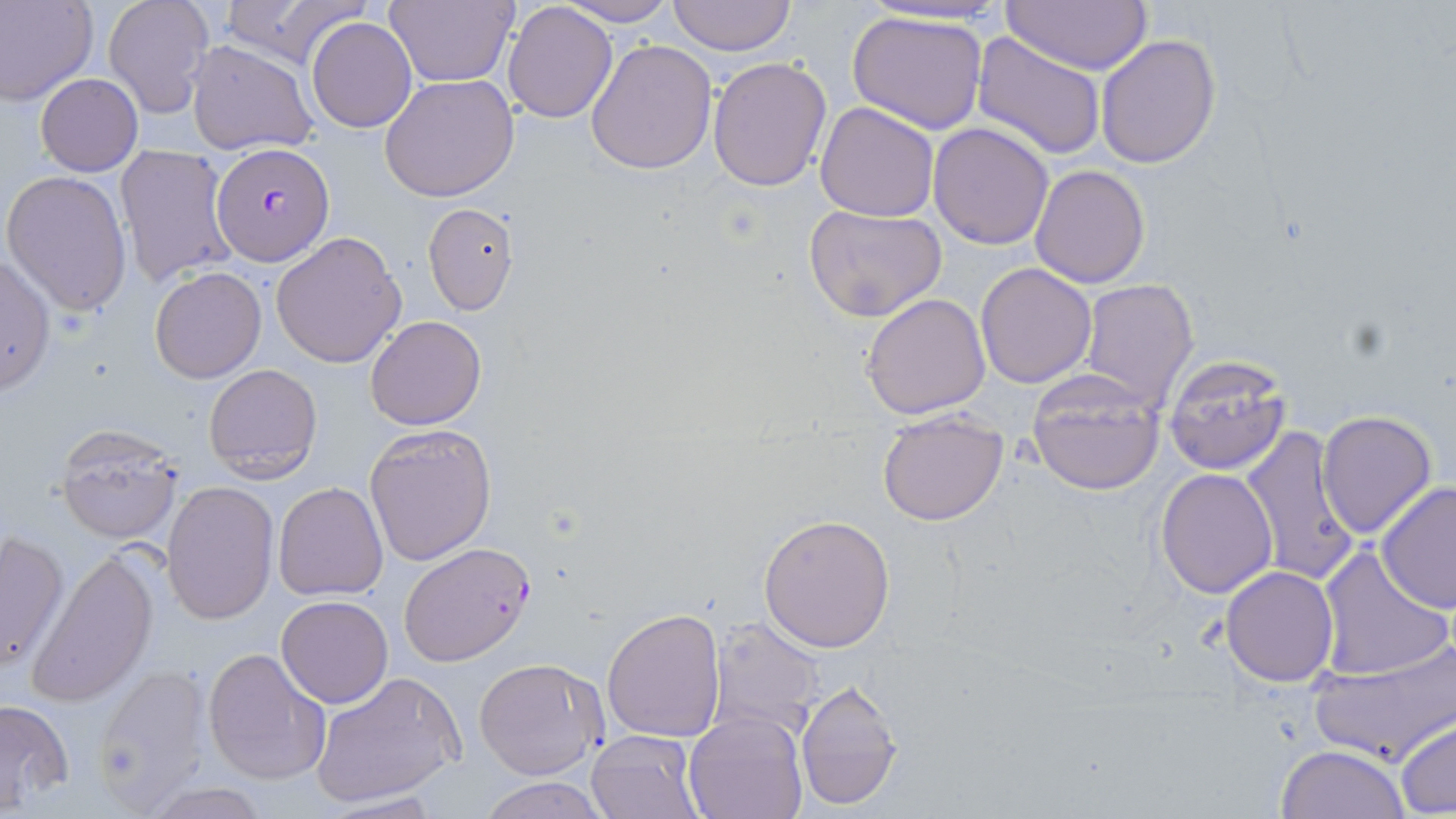
slide-level diagnosis = Plasmodium falciparum
stain = May-Grünwald-Giemsa
uninfected red blood cell locations = approximate bounding boxes as (x1, y1, x2, y2) in pixels: (0, 0, 97, 105), (217, 0, 371, 71), (385, 0, 514, 88), (666, 0, 797, 55), (101, 1, 214, 117), (558, 1, 677, 26), (999, 1, 1152, 73), (501, 3, 617, 122), (845, 9, 989, 134), (305, 18, 417, 133), (973, 33, 1107, 161), (1095, 35, 1221, 170), (585, 38, 717, 176), (185, 40, 317, 155), (707, 55, 832, 193), (34, 72, 143, 174), (379, 75, 519, 203), (815, 101, 941, 220), (928, 121, 1055, 249), (114, 146, 239, 290), (1031, 164, 1150, 288), (3, 169, 132, 317), (421, 202, 519, 315), (804, 204, 946, 322), (270, 230, 406, 368), (0, 254, 56, 394), (975, 262, 1097, 388), (150, 266, 267, 383), (1079, 278, 1199, 408), (861, 293, 991, 419), (365, 316, 487, 430), (1162, 353, 1292, 475), (202, 362, 323, 485), (1028, 369, 1166, 495), (1317, 410, 1438, 541), (877, 411, 1009, 527), (54, 422, 186, 543), (363, 423, 495, 565), (1240, 428, 1363, 587), (1155, 468, 1278, 597), (161, 481, 279, 624), (274, 481, 388, 601), (1374, 481, 1455, 614), (759, 514, 895, 652), (1, 529, 69, 673), (28, 547, 159, 706), (1316, 547, 1452, 682), (1221, 566, 1339, 686), (276, 596, 392, 707), (603, 609, 726, 742), (705, 615, 824, 741), (1310, 639, 1454, 765), (202, 647, 331, 786), (473, 656, 607, 779), (91, 663, 211, 813), (308, 670, 465, 809), (794, 684, 904, 811), (0, 699, 73, 813), (684, 712, 807, 819), (1394, 720, 1456, 814), (586, 730, 702, 818), (1274, 745, 1411, 819), (476, 777, 612, 819), (140, 782, 274, 818), (315, 793, 447, 819)
Plasmodium falciparum-infected red blood cell locations = approximate bounding boxes as (x1, y1, x2, y2) in pixels: (212, 144, 333, 266), (398, 542, 535, 666)
preparation = thin blood smear
field of view = single
modality = optical microscopy
magnification = 1000x
image size = 1456×819 pixels